Classify this cell by malaria status.
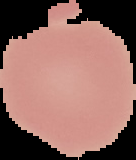

Uninfected.

Image is 136×160 pixels. From a thin blood film. Cell region segmented out of the field of view; the surrounding area is masked to black.